Name the parasite shown.
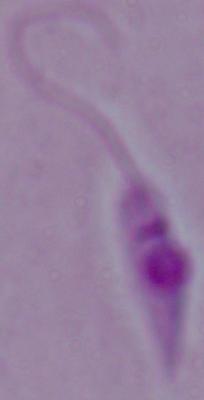

This is Leishmania.

1000x magnification. Photomicrograph.